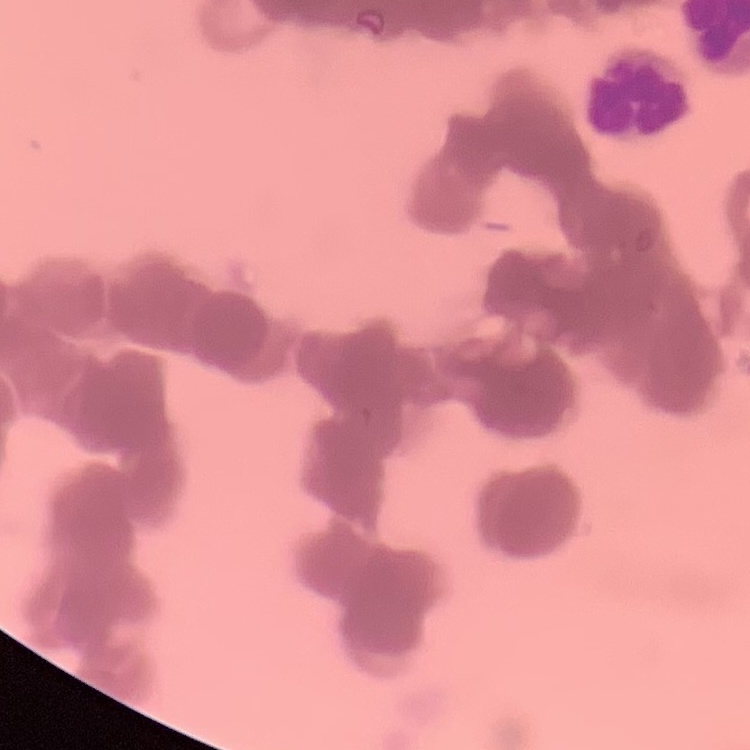
{
  "erythrocyte_morphology": "rouleaux formation",
  "image_type": "one tile cut from a larger photomicrograph",
  "preparation": "thin blood film",
  "stain": "Field's or Giemsa"
}